Report the malaria status of this cell.
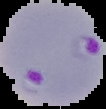

Parasitized.

Summary:
  - Preparation: thin blood film
  - Image type: segmented cell region with the area outside set to black
  - Image size: 106×109 pixels